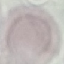

malaria_status: uninfected
stain: Giemsa
capture: smartphone camera at the microscope eyepiece
preparation: thin smear
image_type: automatically extracted cell patch, resized to 64 × 64 pixels